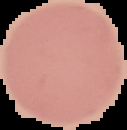 Segmented cell region on a black background. Image is 127×130 pixels. Result: no malaria parasites seen. From a thin blood film.